Report the malaria status of this cell.
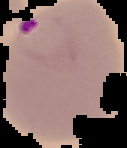
It is parasitized.

Summary:
  - Image size: 127×148 pixels
  - Image type: segmented cell region on a black background
  - Preparation: thin blood film